Describe the morphology of the red blood cells.
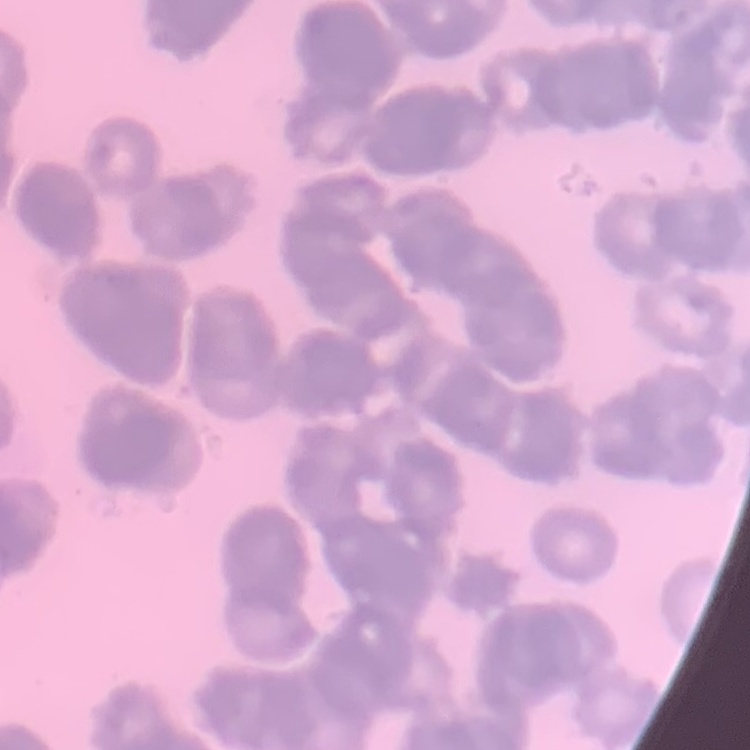

Rouleaux formation.

Summary:
  - Preparation: thin peripheral smear
  - Stain: Field's or Giemsa
  - Image type: one tile cut from a larger photomicrograph